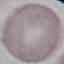

malaria status = uninfected
image type = cell patch, automatically extracted from a larger field of view and resized to 64 × 64 pixels
capture = smartphone through the microscope eyepiece
preparation = thin blood film
stain = Giemsa